Report the malaria status of this cell.
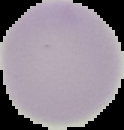
Uninfected.

Segmented cell region on a black background. From a thin blood film. Image is 124×130 pixels.